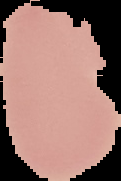

Summary:
  - Result: no Plasmodium parasites seen
  - Image size: 121×181 pixels
  - Image type: segmented cell region with the area outside set to black
  - Preparation: thin blood smear